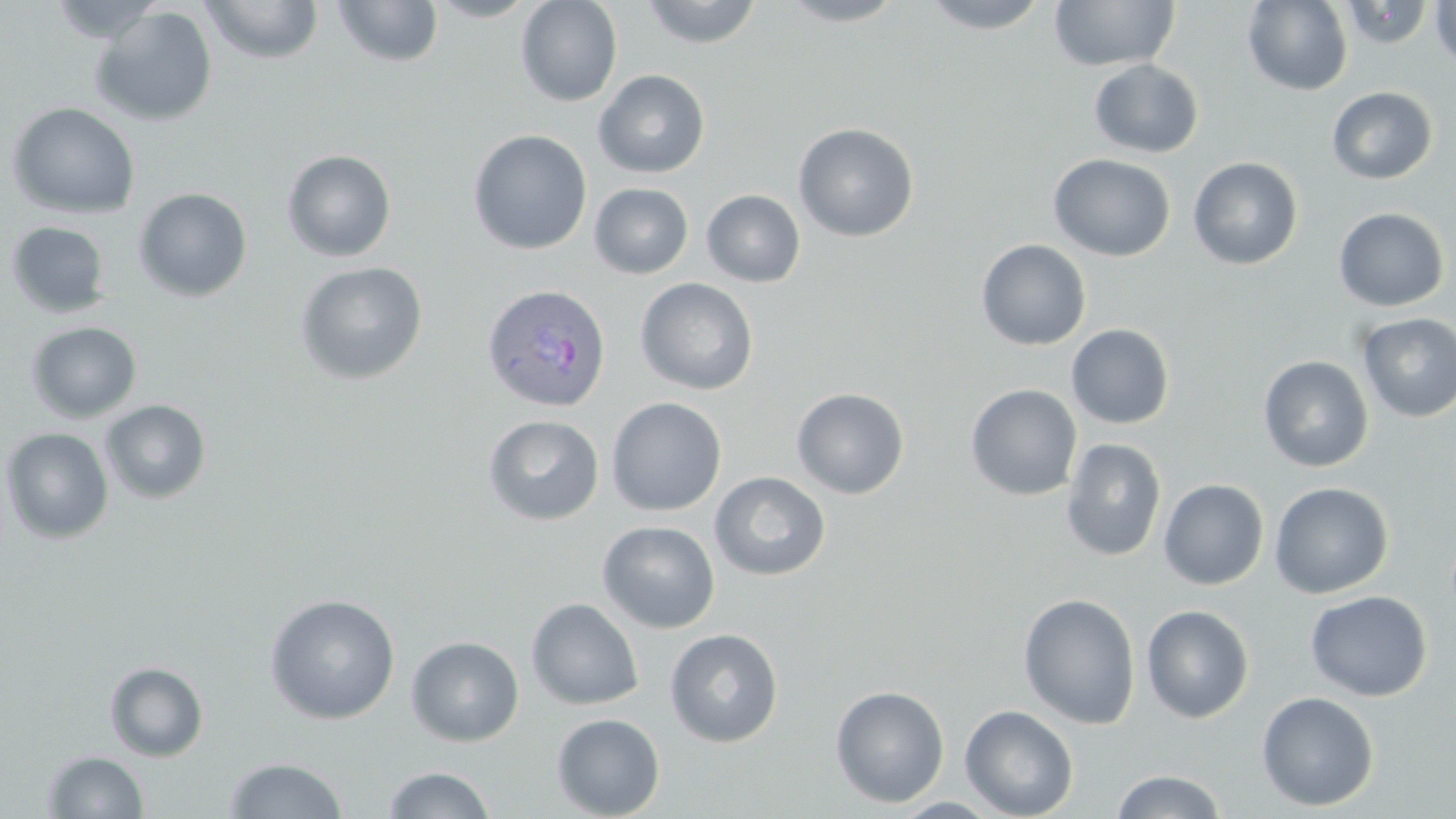
Summary:
  - Coordinate format: approximate bounding boxes as named x1/y1/x2/y2 corners in pixels
  - Uninfected red blood cell locations: (x1=47, y1=0, x2=165, y2=43), (x1=201, y1=0, x2=324, y2=64), (x1=425, y1=0, x2=540, y2=22), (x1=516, y1=0, x2=623, y2=107), (x1=639, y1=0, x2=764, y2=48), (x1=776, y1=0, x2=908, y2=27), (x1=917, y1=0, x2=1053, y2=33), (x1=1048, y1=0, x2=1180, y2=71), (x1=1242, y1=0, x2=1353, y2=96), (x1=1431, y1=0, x2=1456, y2=73), (x1=332, y1=1, x2=444, y2=68), (x1=90, y1=5, x2=218, y2=127), (x1=1088, y1=59, x2=1204, y2=158), (x1=594, y1=69, x2=710, y2=178), (x1=1327, y1=86, x2=1438, y2=185), (x1=6, y1=102, x2=140, y2=219), (x1=793, y1=122, x2=920, y2=243), (x1=468, y1=129, x2=592, y2=255), (x1=281, y1=150, x2=397, y2=262), (x1=1048, y1=154, x2=1176, y2=261), (x1=1187, y1=156, x2=1303, y2=270), (x1=589, y1=183, x2=693, y2=279), (x1=133, y1=187, x2=253, y2=302), (x1=702, y1=189, x2=805, y2=287), (x1=1332, y1=207, x2=1451, y2=311), (x1=5, y1=220, x2=112, y2=318), (x1=975, y1=239, x2=1091, y2=351), (x1=294, y1=261, x2=429, y2=385), (x1=635, y1=278, x2=758, y2=395), (x1=1357, y1=313, x2=1456, y2=422), (x1=26, y1=321, x2=142, y2=423), (x1=1066, y1=323, x2=1175, y2=430), (x1=1258, y1=355, x2=1374, y2=473), (x1=965, y1=383, x2=1083, y2=501), (x1=791, y1=388, x2=910, y2=499), (x1=606, y1=397, x2=727, y2=516), (x1=100, y1=399, x2=212, y2=504), (x1=483, y1=415, x2=604, y2=525), (x1=1, y1=427, x2=114, y2=544), (x1=1060, y1=438, x2=1167, y2=562), (x1=709, y1=471, x2=831, y2=581), (x1=1158, y1=479, x2=1269, y2=590), (x1=1269, y1=482, x2=1393, y2=598), (x1=597, y1=520, x2=720, y2=633), (x1=1305, y1=590, x2=1432, y2=701), (x1=1018, y1=592, x2=1141, y2=729), (x1=264, y1=593, x2=401, y2=724), (x1=526, y1=598, x2=644, y2=710), (x1=1141, y1=605, x2=1255, y2=724), (x1=664, y1=628, x2=784, y2=747), (x1=406, y1=636, x2=524, y2=747), (x1=104, y1=662, x2=209, y2=761), (x1=830, y1=684, x2=950, y2=808), (x1=1256, y1=691, x2=1380, y2=812), (x1=960, y1=704, x2=1079, y2=819), (x1=551, y1=713, x2=665, y2=819), (x1=42, y1=750, x2=149, y2=818), (x1=223, y1=756, x2=348, y2=818), (x1=381, y1=766, x2=495, y2=818), (x1=1110, y1=769, x2=1228, y2=818), (x1=891, y1=797, x2=1002, y2=818)
  - Plasmodium ovale-infected red blood cell locations: (x1=481, y1=283, x2=612, y2=413)
  - Slide-level diagnosis: Plasmodium ovale
  - Field of view: one of a larger specimen
  - Magnification: 1000x
  - Stain: May-Grünwald-Giemsa
  - Modality: optical microscopy
  - Image size: 1456×819 pixels
  - Preparation: thin blood film